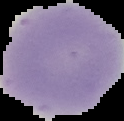

malaria status = uninfected
preparation = thin blood film
image type = cell region segmented out of the field of view; surrounding area masked to black
image size = 124×121 pixels